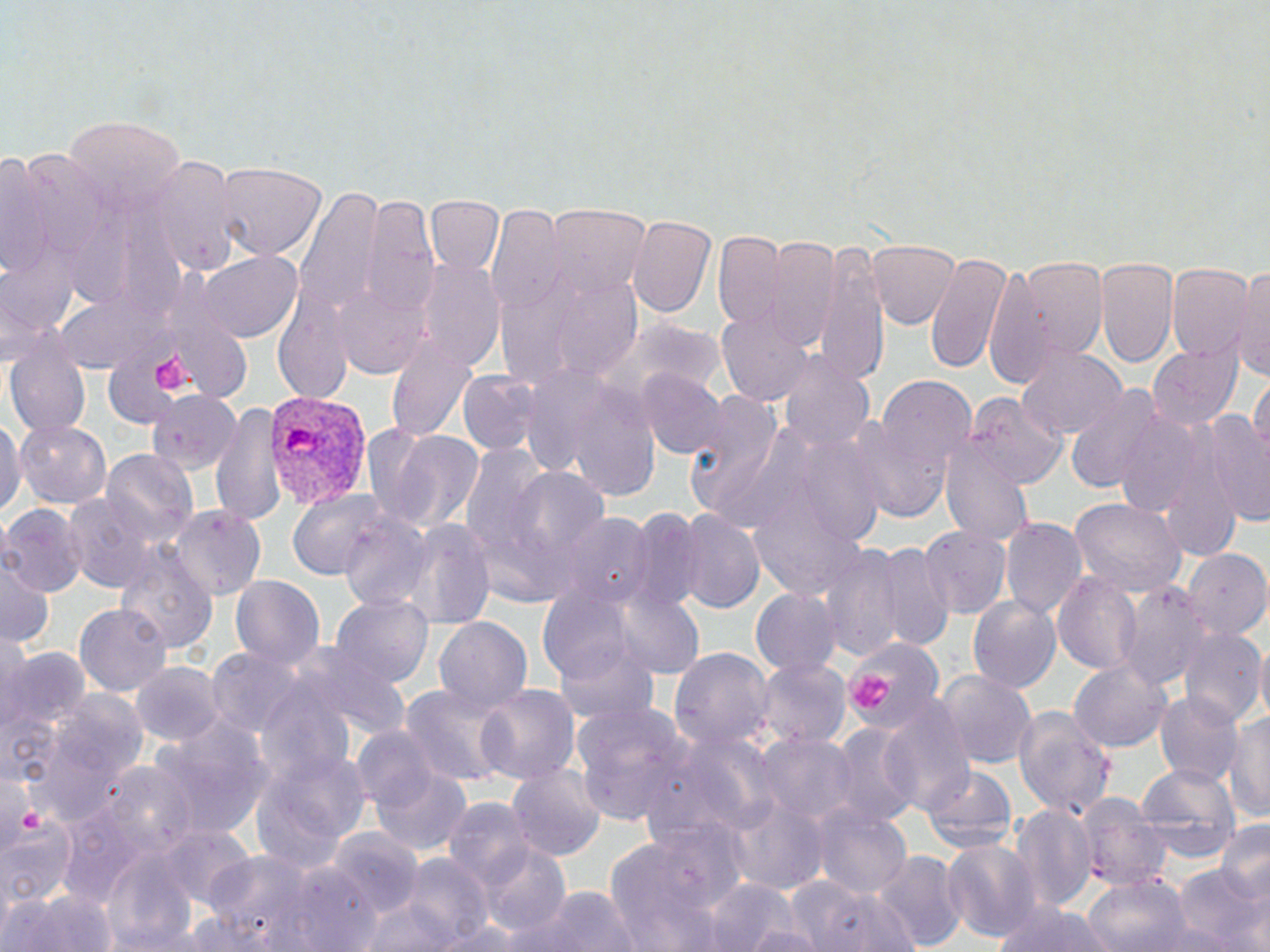
Plasmodium vivax-infected red blood cell locations = approximate bounding boxes as named x1/y1/x2/y2 corners in pixels: (x1=260, y1=388, x2=372, y2=511)
slide-level diagnosis = Plasmodium vivax
preparation = thin blood film
uninfected red blood cell locations = approximate bounding boxes as named x1/y1/x2/y2 corners in pixels: (x1=60, y1=114, x2=183, y2=218), (x1=2, y1=149, x2=53, y2=289), (x1=147, y1=158, x2=238, y2=275), (x1=216, y1=161, x2=328, y2=263), (x1=298, y1=185, x2=384, y2=313), (x1=426, y1=194, x2=505, y2=276), (x1=361, y1=195, x2=436, y2=316), (x1=545, y1=205, x2=650, y2=299), (x1=490, y1=208, x2=569, y2=315), (x1=627, y1=214, x2=719, y2=321), (x1=714, y1=231, x2=787, y2=330), (x1=769, y1=236, x2=840, y2=352), (x1=809, y1=236, x2=888, y2=387), (x1=867, y1=237, x2=959, y2=330), (x1=925, y1=248, x2=1011, y2=375), (x1=194, y1=251, x2=305, y2=343), (x1=418, y1=257, x2=504, y2=368), (x1=1012, y1=257, x2=1105, y2=367), (x1=1094, y1=257, x2=1179, y2=371), (x1=982, y1=260, x2=1065, y2=391), (x1=1167, y1=264, x2=1253, y2=362), (x1=1234, y1=267, x2=1269, y2=381), (x1=336, y1=276, x2=426, y2=378), (x1=547, y1=278, x2=646, y2=381), (x1=272, y1=286, x2=353, y2=406), (x1=718, y1=310, x2=815, y2=407), (x1=5, y1=329, x2=90, y2=438), (x1=387, y1=333, x2=479, y2=443), (x1=1149, y1=342, x2=1244, y2=429), (x1=1017, y1=346, x2=1125, y2=440), (x1=778, y1=352, x2=876, y2=454), (x1=639, y1=370, x2=723, y2=460), (x1=456, y1=371, x2=540, y2=458), (x1=561, y1=371, x2=665, y2=503), (x1=1251, y1=372, x2=1270, y2=466), (x1=871, y1=373, x2=978, y2=498), (x1=1064, y1=384, x2=1167, y2=496), (x1=144, y1=388, x2=242, y2=479), (x1=683, y1=389, x2=794, y2=525), (x1=965, y1=392, x2=1069, y2=490), (x1=208, y1=398, x2=286, y2=528), (x1=1115, y1=406, x2=1213, y2=523), (x1=847, y1=410, x2=957, y2=526), (x1=1200, y1=410, x2=1269, y2=528), (x1=0, y1=412, x2=20, y2=524), (x1=14, y1=420, x2=112, y2=509), (x1=366, y1=424, x2=485, y2=535), (x1=943, y1=439, x2=1033, y2=544), (x1=102, y1=450, x2=197, y2=546), (x1=461, y1=450, x2=609, y2=605), (x1=287, y1=488, x2=391, y2=584), (x1=65, y1=494, x2=159, y2=591), (x1=1070, y1=498, x2=1186, y2=599), (x1=1, y1=504, x2=88, y2=596), (x1=138, y1=504, x2=286, y2=638), (x1=172, y1=507, x2=265, y2=601), (x1=623, y1=510, x2=700, y2=613), (x1=677, y1=512, x2=765, y2=616), (x1=338, y1=513, x2=433, y2=614), (x1=559, y1=513, x2=652, y2=608), (x1=404, y1=519, x2=495, y2=629), (x1=1000, y1=519, x2=1086, y2=620), (x1=917, y1=525, x2=1010, y2=619), (x1=115, y1=540, x2=219, y2=658), (x1=856, y1=542, x2=953, y2=653), (x1=818, y1=543, x2=910, y2=661), (x1=1182, y1=549, x2=1270, y2=642), (x1=0, y1=553, x2=51, y2=652), (x1=1055, y1=572, x2=1140, y2=674), (x1=230, y1=576, x2=324, y2=670), (x1=1116, y1=580, x2=1210, y2=689), (x1=751, y1=587, x2=842, y2=677), (x1=612, y1=589, x2=704, y2=680), (x1=330, y1=594, x2=434, y2=687), (x1=967, y1=595, x2=1064, y2=694), (x1=74, y1=600, x2=169, y2=694), (x1=435, y1=617, x2=532, y2=712), (x1=1179, y1=631, x2=1265, y2=726), (x1=840, y1=637, x2=951, y2=750), (x1=284, y1=638, x2=413, y2=744), (x1=1251, y1=640, x2=1270, y2=722), (x1=672, y1=645, x2=773, y2=752), (x1=3, y1=646, x2=87, y2=738), (x1=206, y1=649, x2=309, y2=738), (x1=1071, y1=660, x2=1172, y2=752), (x1=756, y1=661, x2=849, y2=752), (x1=132, y1=662, x2=227, y2=748), (x1=937, y1=669, x2=1037, y2=768), (x1=475, y1=681, x2=580, y2=786), (x1=402, y1=684, x2=509, y2=789), (x1=36, y1=689, x2=150, y2=819), (x1=1154, y1=691, x2=1244, y2=786), (x1=880, y1=694, x2=976, y2=819), (x1=571, y1=700, x2=693, y2=826), (x1=1012, y1=703, x2=1117, y2=822), (x1=1226, y1=706, x2=1270, y2=822), (x1=153, y1=722, x2=268, y2=837), (x1=829, y1=723, x2=920, y2=828), (x1=351, y1=726, x2=438, y2=818), (x1=756, y1=732, x2=855, y2=826), (x1=248, y1=737, x2=369, y2=879), (x1=369, y1=757, x2=472, y2=857), (x1=1137, y1=763, x2=1238, y2=856), (x1=88, y1=764, x2=201, y2=864), (x1=507, y1=765, x2=604, y2=860), (x1=924, y1=766, x2=1016, y2=853), (x1=1075, y1=792, x2=1166, y2=891), (x1=442, y1=797, x2=536, y2=891), (x1=727, y1=798, x2=827, y2=892), (x1=1012, y1=803, x2=1098, y2=911), (x1=815, y1=805, x2=910, y2=901), (x1=3, y1=809, x2=78, y2=913), (x1=1214, y1=818, x2=1270, y2=913), (x1=163, y1=827, x2=257, y2=909), (x1=327, y1=829, x2=423, y2=916), (x1=606, y1=835, x2=724, y2=952), (x1=941, y1=837, x2=1041, y2=942), (x1=473, y1=846, x2=574, y2=940), (x1=103, y1=849, x2=200, y2=952), (x1=204, y1=849, x2=318, y2=947), (x1=872, y1=851, x2=965, y2=950), (x1=404, y1=854, x2=492, y2=946), (x1=278, y1=864, x2=382, y2=950), (x1=1173, y1=864, x2=1265, y2=951), (x1=1083, y1=873, x2=1188, y2=952), (x1=784, y1=877, x2=879, y2=948), (x1=705, y1=878, x2=798, y2=952), (x1=4, y1=882, x2=116, y2=952), (x1=808, y1=883, x2=923, y2=952), (x1=522, y1=885, x2=642, y2=952), (x1=361, y1=891, x2=464, y2=950), (x1=991, y1=899, x2=1116, y2=952), (x1=749, y1=917, x2=822, y2=952)
field of view = one of a larger specimen
platelet locations = approximate bounding boxes as named x1/y1/x2/y2 corners in pixels: (x1=151, y1=348, x2=195, y2=390), (x1=850, y1=672, x2=896, y2=711)
magnification = 1000x
stain = May-Grünwald-Giemsa
modality = light microscopy
image size = 1270×952 pixels